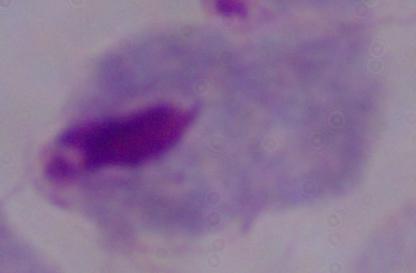 A trichomonad is seen. Micrograph. 1000x magnification.